Give the extent of all Plasmodium parasites.
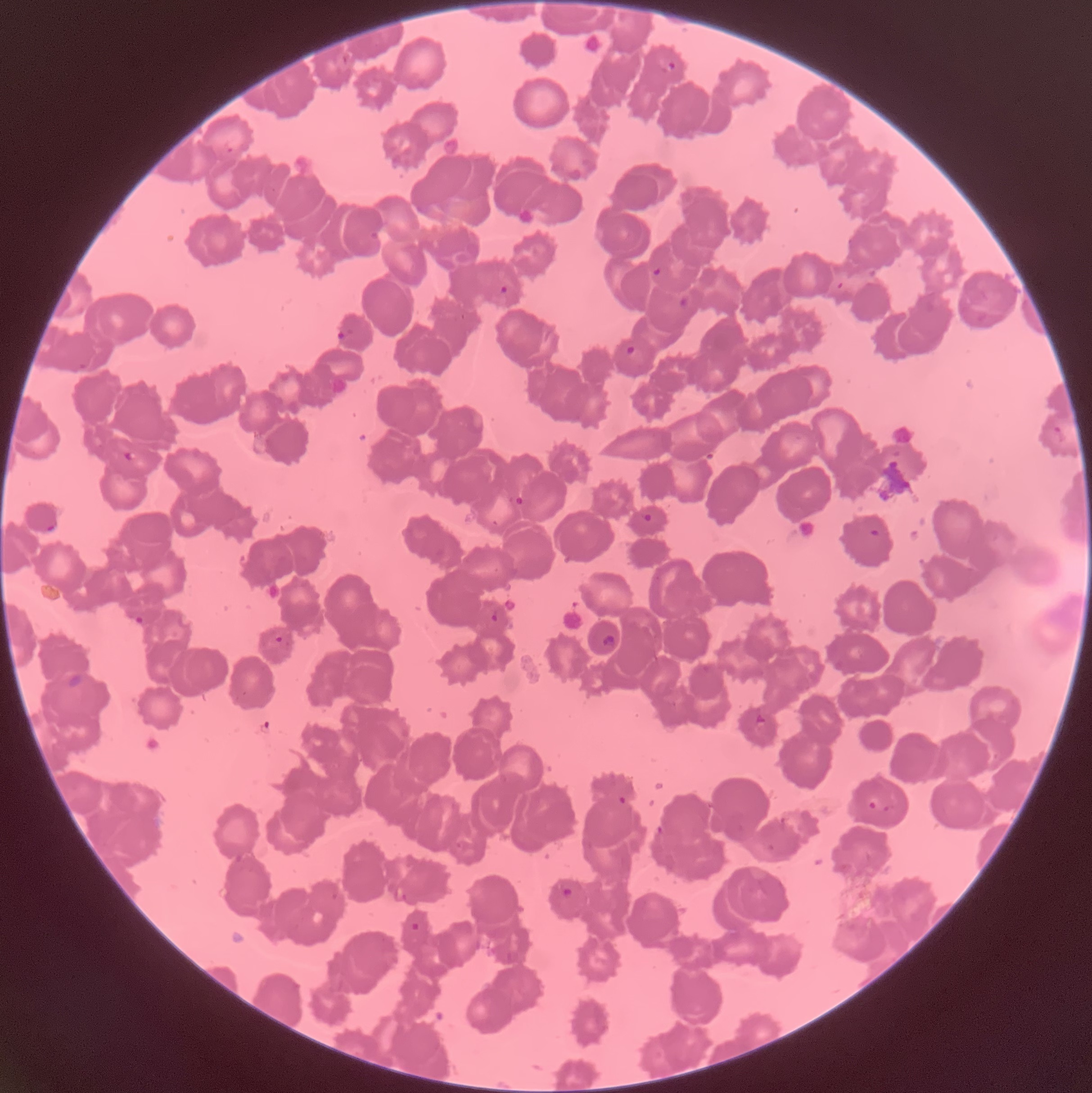
Approximate bounding boxes as (x1,y1)-(x2,y2) corner pairs in pixels.
Plasmodium parasites: (659,56)-(678,74), (652,267)-(661,276), (499,285)-(509,294), (678,296)-(690,307), (338,328)-(355,339), (624,344)-(637,356), (78,361)-(87,370), (1053,425)-(1069,443), (122,451)-(138,461), (514,496)-(524,506), (640,511)-(653,522), (46,524)-(57,533), (868,528)-(880,539), (489,613)-(499,623), (133,616)-(144,626), (275,635)-(284,645), (601,635)-(616,650), (755,714)-(766,724), (618,795)-(628,805), (868,800)-(876,809), (883,804)-(896,812), (656,825)-(664,835), (560,887)-(573,899), (409,920)-(421,932).

Summary:
  - Image size: 1092×1093 pixels
  - Red blood cell morphology: rouleaux formation
  - Preparation: thin blood film
  - Modality: light microscopy